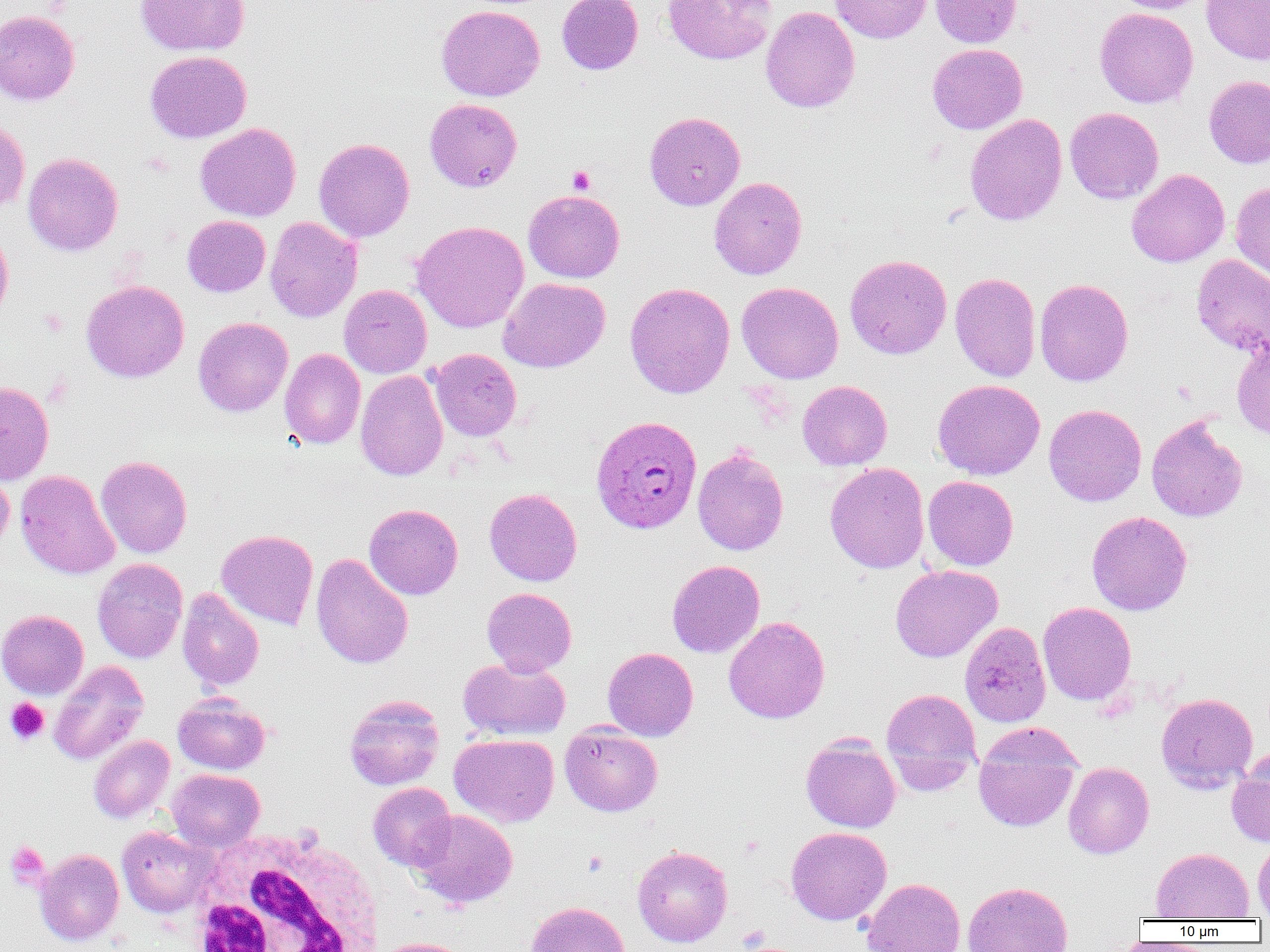
slide-level diagnosis = Plasmodium ovale
uninfected red blood cell locations = approximate bounding boxes as (x1,y1)-(x2,y2) corner pairs in pixels: (135,0)-(250,56), (557,0)-(643,75), (662,0)-(776,64), (830,0)-(932,43), (930,0)-(1022,47), (1110,0)-(1211,13), (1201,0)-(1270,65), (436,5)-(545,101), (760,6)-(860,113), (1095,7)-(1198,108), (0,9)-(80,105), (927,43)-(1027,134), (145,50)-(251,143), (1203,75)-(1270,169), (425,98)-(522,192), (1065,107)-(1164,204), (644,111)-(745,210), (965,114)-(1067,226), (0,117)-(30,213), (196,123)-(301,222), (314,138)-(414,242), (23,153)-(123,256), (1126,169)-(1229,267), (709,177)-(807,280), (1230,182)-(1270,283), (523,190)-(625,283), (182,215)-(270,297), (265,217)-(362,323), (411,220)-(529,333), (0,226)-(13,326), (845,254)-(951,360), (1192,254)-(1270,358), (950,272)-(1040,382), (499,278)-(610,373), (1035,278)-(1134,386), (81,280)-(189,382), (625,282)-(735,399), (737,282)-(844,384), (339,285)-(432,378), (193,317)-(293,417), (1232,342)-(1270,439), (279,348)-(365,449), (430,349)-(521,441), (355,370)-(448,481), (932,379)-(1045,480), (797,380)-(893,470), (0,381)-(54,484), (1043,403)-(1146,506), (1146,415)-(1248,522), (693,448)-(788,556), (96,455)-(192,558), (825,462)-(929,573), (0,465)-(14,555), (15,469)-(119,580), (923,475)-(1018,570), (484,488)-(582,586), (364,503)-(463,600), (1086,511)-(1192,616), (216,529)-(319,630), (311,553)-(413,669), (92,558)-(188,663), (667,560)-(765,658), (890,564)-(1003,662), (481,587)-(577,676), (177,588)-(264,692), (1038,602)-(1136,705), (0,609)-(88,699), (723,616)-(830,723), (959,621)-(1051,727), (603,647)-(698,741), (458,656)-(570,742), (48,660)-(149,766), (881,688)-(982,788), (1156,692)-(1258,792), (173,693)-(270,774), (344,695)-(444,790), (560,724)-(662,817), (449,734)-(559,828), (88,735)-(174,823), (801,735)-(901,833), (973,736)-(1079,832), (1227,751)-(1270,848), (1063,762)-(1154,859), (167,769)-(264,851), (368,782)-(457,870), (409,809)-(518,909), (786,826)-(891,925), (117,827)-(213,917), (1253,838)-(1270,919), (632,845)-(732,947), (1152,847)-(1253,920), (35,849)-(124,945), (861,878)-(965,952), (962,881)-(1073,952), (524,901)-(630,952), (372,937)-(471,952)
image size = 1270×952 pixels
Plasmodium ovale-infected red blood cell locations = approximate bounding boxes as (x1,y1)-(x2,y2) corner pairs in pixels: (590,415)-(702,534)
modality = optical microscopy
magnification = 1000x
field of view = one of a larger specimen
white blood cell locations = approximate bounding boxes as (x1,y1)-(x2,y2) corner pairs in pixels: (185,827)-(385,952)
preparation = thin blood film
platelet locations = approximate bounding boxes as (x1,y1)-(x2,y2) corner pairs in pixels: (567,166)-(595,194), (5,698)-(49,745), (6,841)-(49,889), (582,851)-(608,877)